Locate and identify every blood parasite.
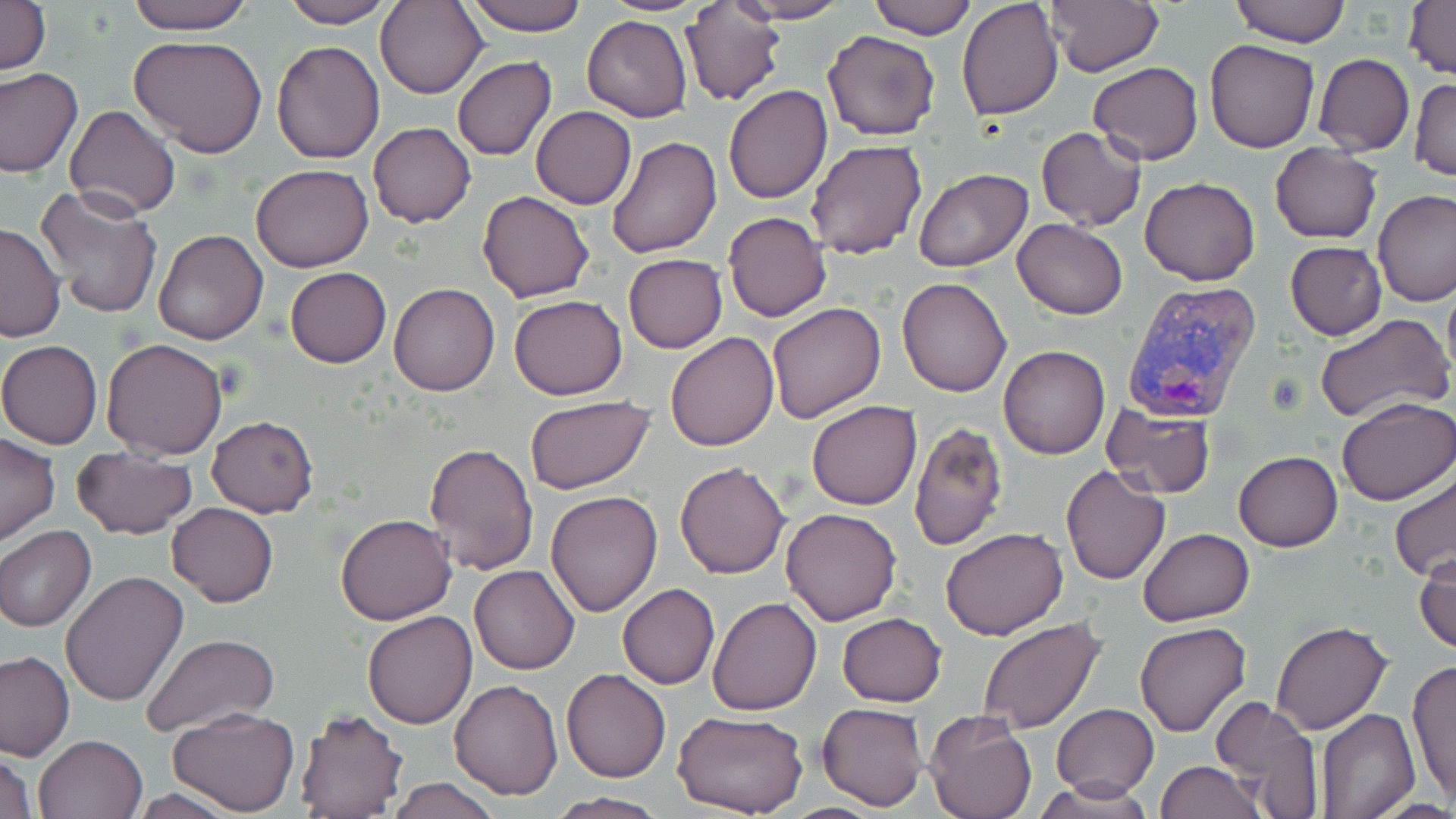

Approximate bounding boxes as named x1/y1/x2/y2 corners in pixels.
Plasmodium vivax-infected red blood cells: (x1=1123, y1=280, x2=1261, y2=424).
No Plasmodium falciparum, Plasmodium ovale, Plasmodium malariae, Babesia divergens, or Trypanosoma brucei observed.

Uninfected red blood cell locations: (x1=0, y1=0, x2=50, y2=77), (x1=123, y1=0, x2=256, y2=35), (x1=375, y1=0, x2=489, y2=100), (x1=463, y1=0, x2=584, y2=36), (x1=595, y1=0, x2=713, y2=16), (x1=730, y1=0, x2=854, y2=23), (x1=864, y1=0, x2=976, y2=40), (x1=957, y1=0, x2=1063, y2=120), (x1=1045, y1=0, x2=1165, y2=77), (x1=1230, y1=0, x2=1348, y2=47), (x1=1403, y1=0, x2=1455, y2=81), (x1=276, y1=1, x2=396, y2=29), (x1=682, y1=3, x2=786, y2=106), (x1=582, y1=15, x2=692, y2=121), (x1=823, y1=31, x2=941, y2=141), (x1=128, y1=35, x2=268, y2=157), (x1=1203, y1=38, x2=1320, y2=153), (x1=272, y1=41, x2=384, y2=164), (x1=1314, y1=53, x2=1415, y2=156), (x1=453, y1=57, x2=556, y2=161), (x1=1087, y1=62, x2=1204, y2=164), (x1=0, y1=67, x2=82, y2=180), (x1=1410, y1=77, x2=1456, y2=182), (x1=723, y1=85, x2=832, y2=204), (x1=63, y1=104, x2=181, y2=218), (x1=531, y1=106, x2=636, y2=210), (x1=368, y1=122, x2=475, y2=228), (x1=1035, y1=125, x2=1146, y2=231), (x1=606, y1=136, x2=722, y2=258), (x1=805, y1=138, x2=929, y2=260), (x1=1270, y1=142, x2=1382, y2=243), (x1=251, y1=164, x2=375, y2=274), (x1=915, y1=168, x2=1034, y2=272), (x1=1139, y1=176, x2=1262, y2=285), (x1=33, y1=185, x2=165, y2=320), (x1=1373, y1=189, x2=1456, y2=307), (x1=478, y1=190, x2=595, y2=302), (x1=724, y1=212, x2=830, y2=321), (x1=1011, y1=218, x2=1128, y2=320), (x1=0, y1=222, x2=66, y2=342), (x1=154, y1=229, x2=269, y2=345), (x1=1285, y1=241, x2=1387, y2=340), (x1=622, y1=254, x2=727, y2=353), (x1=285, y1=266, x2=391, y2=368), (x1=897, y1=278, x2=1013, y2=398), (x1=389, y1=284, x2=499, y2=397), (x1=509, y1=295, x2=628, y2=401), (x1=766, y1=301, x2=886, y2=422), (x1=1315, y1=313, x2=1452, y2=423), (x1=677, y1=317, x2=881, y2=436), (x1=665, y1=332, x2=779, y2=451), (x1=101, y1=337, x2=229, y2=460), (x1=0, y1=339, x2=103, y2=450), (x1=998, y1=347, x2=1110, y2=460), (x1=526, y1=395, x2=656, y2=492), (x1=1336, y1=396, x2=1455, y2=505), (x1=806, y1=400, x2=922, y2=511), (x1=1101, y1=401, x2=1215, y2=499), (x1=207, y1=416, x2=318, y2=517), (x1=909, y1=421, x2=1009, y2=551), (x1=0, y1=433, x2=60, y2=545), (x1=423, y1=442, x2=539, y2=574), (x1=73, y1=447, x2=197, y2=539), (x1=1234, y1=451, x2=1343, y2=552), (x1=675, y1=460, x2=791, y2=578), (x1=1060, y1=465, x2=1171, y2=584), (x1=1390, y1=472, x2=1456, y2=584), (x1=545, y1=490, x2=662, y2=617), (x1=168, y1=501, x2=278, y2=607), (x1=780, y1=508, x2=903, y2=626), (x1=335, y1=513, x2=458, y2=625), (x1=0, y1=526, x2=96, y2=633), (x1=941, y1=527, x2=1069, y2=641), (x1=1138, y1=529, x2=1253, y2=626), (x1=8, y1=534, x2=150, y2=668), (x1=1414, y1=545, x2=1456, y2=655), (x1=470, y1=565, x2=579, y2=675), (x1=60, y1=570, x2=189, y2=707), (x1=618, y1=584, x2=719, y2=689), (x1=707, y1=595, x2=820, y2=715), (x1=362, y1=611, x2=479, y2=729), (x1=836, y1=612, x2=947, y2=707), (x1=976, y1=617, x2=1106, y2=735), (x1=1134, y1=620, x2=1252, y2=737), (x1=1270, y1=620, x2=1395, y2=735), (x1=141, y1=633, x2=280, y2=736), (x1=0, y1=649, x2=74, y2=760), (x1=1406, y1=658, x2=1456, y2=807), (x1=561, y1=668, x2=672, y2=783), (x1=448, y1=680, x2=564, y2=801), (x1=1209, y1=696, x2=1326, y2=818), (x1=818, y1=702, x2=928, y2=811), (x1=1052, y1=703, x2=1159, y2=799), (x1=166, y1=706, x2=299, y2=816), (x1=294, y1=708, x2=408, y2=818), (x1=1316, y1=710, x2=1420, y2=819), (x1=673, y1=712, x2=807, y2=818), (x1=925, y1=715, x2=1036, y2=819), (x1=34, y1=733, x2=147, y2=818), (x1=0, y1=749, x2=38, y2=819), (x1=1156, y1=761, x2=1265, y2=819), (x1=388, y1=777, x2=504, y2=819), (x1=1038, y1=778, x2=1152, y2=816), (x1=125, y1=787, x2=244, y2=818), (x1=549, y1=792, x2=669, y2=818). Slide-level diagnosis: Plasmodium vivax. Single field of view. May-Grünwald-Giemsa stain. Light microscopy. 1000x magnification. Image is 1456×819 pixels. Thin blood smear.